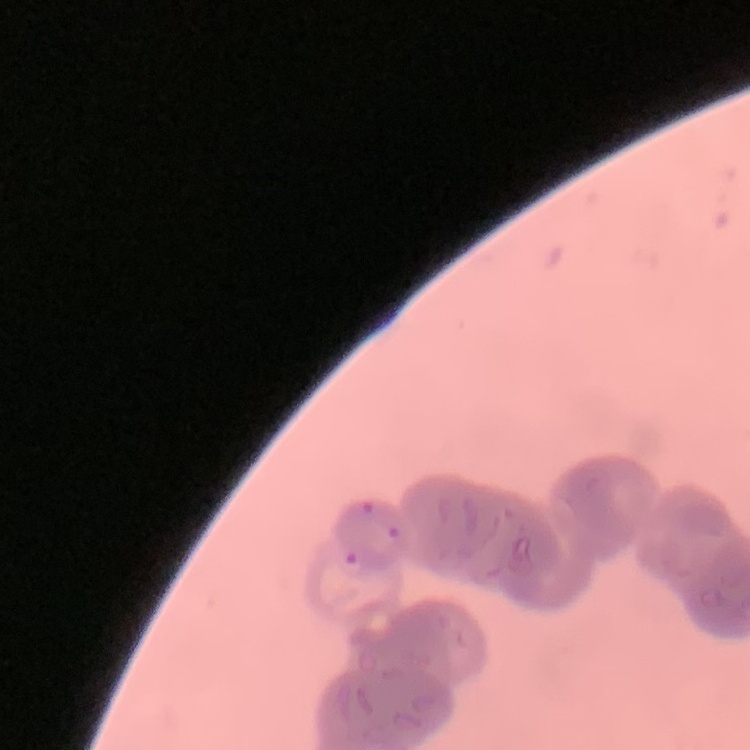
erythrocyte_morphology: rouleaux formation
stain: Field's or Giemsa
preparation: thin peripheral smear
image_type: square crop of a larger photomicrograph